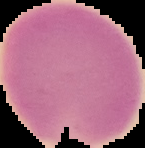
Cell region segmented out of the field of view; the surrounding area is masked to black. Malaria status: uninfected. Image is 145×148 pixels. From a thin blood smear.